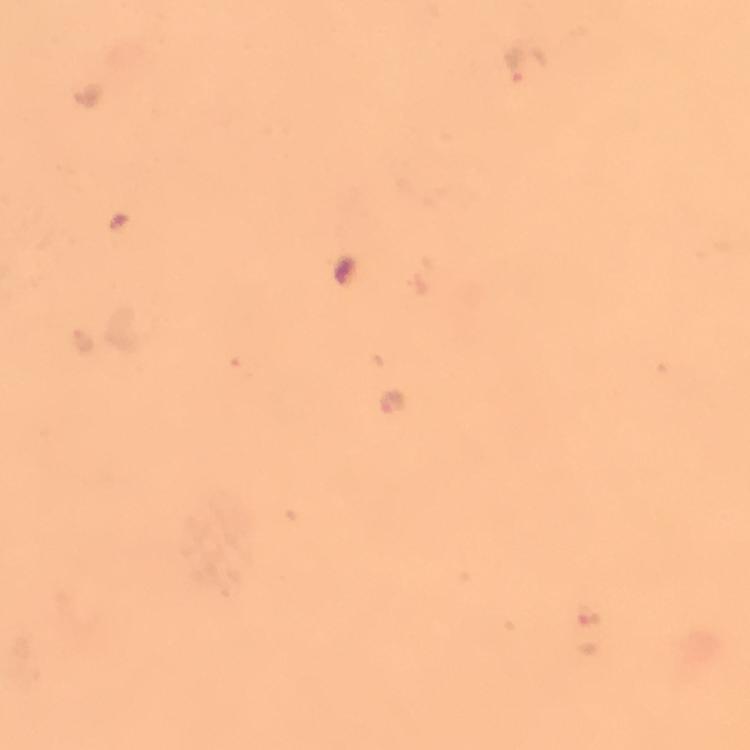

context: from a malaria diagnostic workup
immersion_oil: used
stain: Giemsa
cropped_from: a single field of view
magnification: 100x
malaria_parasite_locations: 'approximate centers as [x, y] in pixels: [527, 62], [81, 339], [391, 401]'
preparation: thick blood smear
capture: smartphone mounted on the microscope
image_size: 750×750 pixels